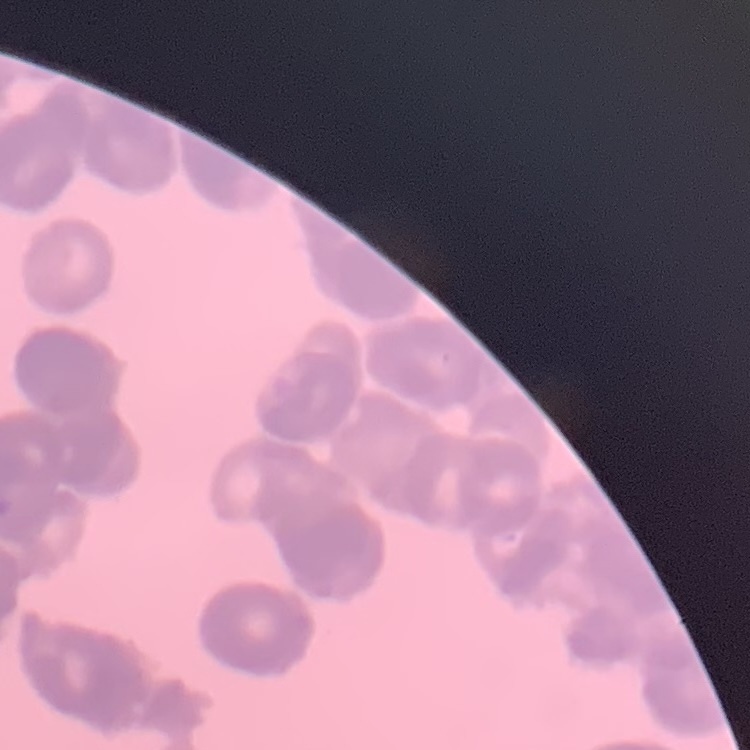
{
  "red_blood_cell_morphology": "rouleaux formation",
  "preparation": "thin blood smear",
  "stain": "Field's or Giemsa",
  "image_type": "square crop of a larger photomicrograph"
}